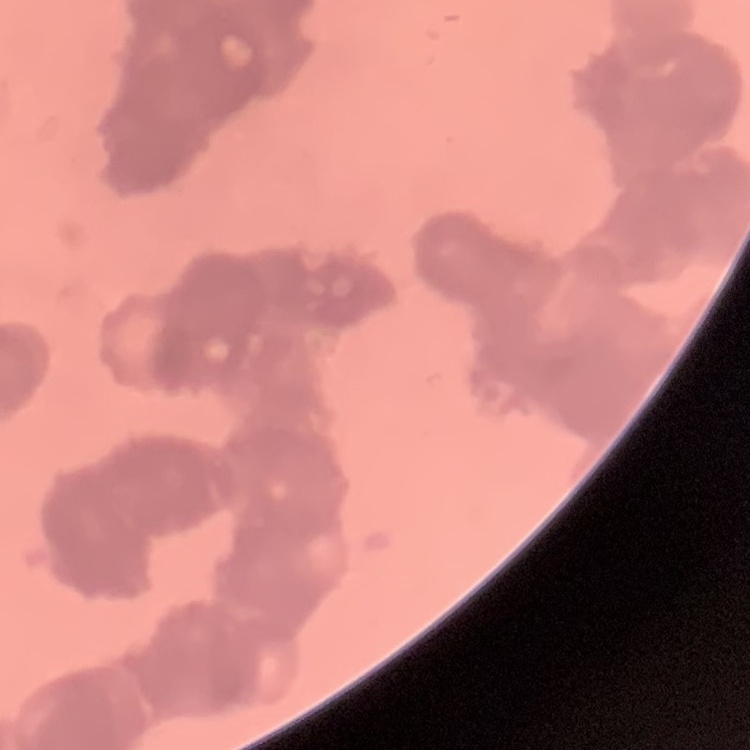

The red blood cells show rouleaux formation. Thin blood film. Field's or Giemsa stain. One tile cut from a larger photomicrograph.